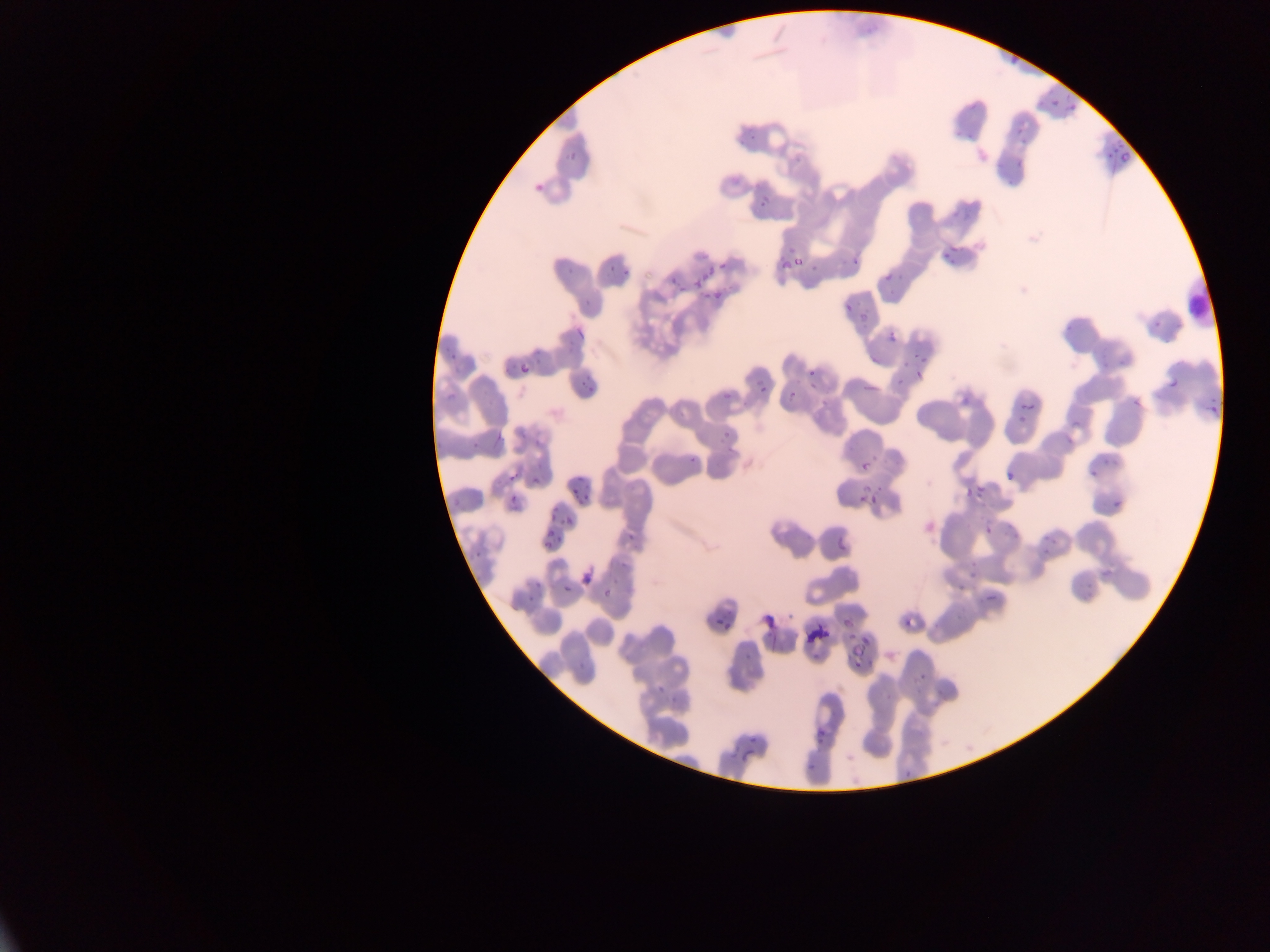
Approximate bounding boxes as (left, top, right, bottom) in pixels. Malaria parasite locations: (1010, 45, 1028, 65), (1043, 95, 1056, 108), (1063, 99, 1079, 115), (1010, 121, 1027, 141), (1106, 139, 1123, 167), (564, 143, 584, 165), (1002, 153, 1023, 169), (531, 180, 547, 192), (761, 197, 770, 206), (938, 247, 958, 267), (796, 251, 802, 272), (850, 254, 861, 271), (604, 255, 621, 275), (779, 259, 790, 270), (719, 262, 728, 271), (690, 264, 711, 291), (809, 265, 819, 273), (564, 267, 577, 276), (664, 274, 681, 294), (714, 292, 723, 301), (844, 302, 852, 311), (1147, 317, 1158, 333), (575, 328, 585, 338), (888, 332, 896, 342), (907, 339, 927, 360), (444, 353, 459, 372), (521, 365, 530, 374), (1166, 366, 1180, 392), (808, 368, 816, 377), (578, 369, 602, 393), (915, 371, 924, 382), (891, 374, 903, 386), (865, 381, 875, 392), (718, 385, 734, 405), (759, 385, 766, 393), (446, 389, 456, 404), (1205, 396, 1221, 414), (1126, 399, 1138, 407), (1023, 401, 1033, 411), (1070, 416, 1082, 432), (721, 421, 737, 445), (530, 429, 544, 445), (467, 439, 479, 456), (686, 447, 701, 467), (1100, 457, 1120, 474), (859, 462, 868, 472), (1002, 469, 1015, 479), (1087, 471, 1096, 480), (507, 472, 517, 482), (566, 474, 587, 494), (963, 484, 982, 505), (872, 488, 883, 499), (1108, 491, 1125, 511), (577, 495, 598, 504), (858, 495, 866, 503), (505, 497, 525, 508), (547, 503, 558, 517), (563, 516, 573, 526), (835, 520, 854, 551), (1013, 520, 1020, 534), (625, 525, 644, 542), (984, 525, 993, 535), (1046, 526, 1057, 545), (545, 535, 555, 547), (963, 547, 977, 576), (472, 548, 484, 566), (615, 563, 626, 572), (1098, 566, 1113, 579), (579, 567, 592, 592), (954, 578, 968, 596), (563, 584, 571, 593), (523, 587, 540, 603), (603, 587, 614, 600), (982, 591, 994, 600), (759, 606, 778, 630), (835, 611, 855, 632), (707, 612, 729, 630), (902, 618, 913, 627), (807, 620, 827, 650), (838, 643, 866, 663), (812, 730, 824, 749), (745, 735, 760, 751), (747, 735, 757, 745), (731, 750, 744, 761) | approximate (x, y) pixel centers of objects too small to bound: (793, 394). One field of view. Sample from Ghana. Image is 1270×952 pixels. Photographed through a microscope with a mobile-phone camera. Thin blood film.